Name the blood parasite species.
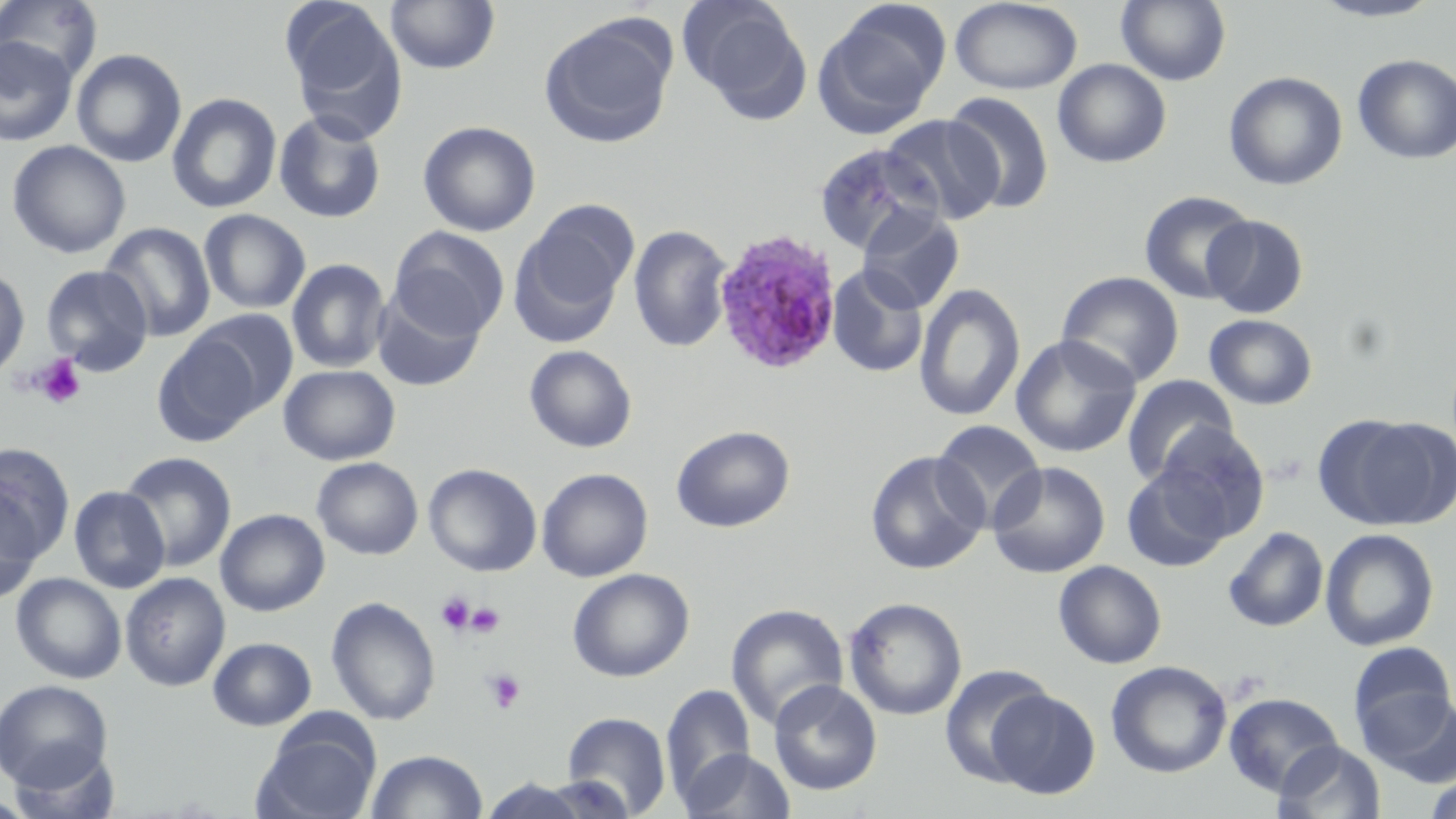
Plasmodium ovale.

Approximate bounding boxes as named x1/y1/x2/y2 corners in pixels. Uninfected red blood cell locations: (x1=0, y1=0, x2=103, y2=83), (x1=281, y1=0, x2=409, y2=142), (x1=385, y1=0, x2=500, y2=75), (x1=1116, y1=0, x2=1231, y2=85), (x1=1308, y1=0, x2=1446, y2=23), (x1=678, y1=1, x2=812, y2=118), (x1=813, y1=1, x2=950, y2=136), (x1=950, y1=1, x2=1083, y2=95), (x1=539, y1=15, x2=677, y2=149), (x1=0, y1=36, x2=78, y2=146), (x1=71, y1=48, x2=187, y2=168), (x1=1353, y1=53, x2=1456, y2=164), (x1=1052, y1=58, x2=1172, y2=168), (x1=1223, y1=71, x2=1348, y2=190), (x1=167, y1=92, x2=282, y2=214), (x1=944, y1=92, x2=1055, y2=215), (x1=273, y1=110, x2=387, y2=224), (x1=881, y1=114, x2=1005, y2=225), (x1=417, y1=120, x2=541, y2=237), (x1=6, y1=140, x2=131, y2=259), (x1=813, y1=143, x2=941, y2=256), (x1=1138, y1=190, x2=1257, y2=304), (x1=857, y1=205, x2=965, y2=313), (x1=511, y1=206, x2=637, y2=343), (x1=199, y1=209, x2=311, y2=314), (x1=1202, y1=214, x2=1309, y2=319), (x1=100, y1=222, x2=216, y2=342), (x1=628, y1=224, x2=734, y2=353), (x1=389, y1=226, x2=509, y2=340), (x1=286, y1=258, x2=391, y2=373), (x1=41, y1=264, x2=153, y2=375), (x1=826, y1=264, x2=928, y2=378), (x1=0, y1=265, x2=30, y2=379), (x1=1056, y1=271, x2=1185, y2=388), (x1=914, y1=283, x2=1026, y2=422), (x1=371, y1=291, x2=485, y2=392), (x1=187, y1=309, x2=299, y2=417), (x1=1204, y1=314, x2=1317, y2=410), (x1=152, y1=334, x2=263, y2=446), (x1=1010, y1=334, x2=1142, y2=458), (x1=524, y1=344, x2=637, y2=453), (x1=279, y1=364, x2=400, y2=465), (x1=1121, y1=374, x2=1238, y2=485), (x1=1319, y1=414, x2=1454, y2=530), (x1=931, y1=420, x2=1046, y2=529), (x1=1153, y1=423, x2=1270, y2=541), (x1=671, y1=425, x2=795, y2=532), (x1=0, y1=444, x2=75, y2=560), (x1=119, y1=451, x2=236, y2=572), (x1=865, y1=451, x2=989, y2=574), (x1=312, y1=456, x2=423, y2=560), (x1=987, y1=460, x2=1111, y2=579), (x1=423, y1=463, x2=542, y2=576), (x1=1121, y1=465, x2=1232, y2=572), (x1=537, y1=468, x2=653, y2=582), (x1=68, y1=485, x2=169, y2=593), (x1=0, y1=489, x2=42, y2=604), (x1=215, y1=509, x2=329, y2=616), (x1=1223, y1=526, x2=1329, y2=632), (x1=1320, y1=528, x2=1439, y2=651), (x1=1053, y1=560, x2=1166, y2=669), (x1=567, y1=568, x2=694, y2=682), (x1=120, y1=572, x2=230, y2=691), (x1=11, y1=573, x2=127, y2=684), (x1=326, y1=596, x2=440, y2=725), (x1=844, y1=597, x2=967, y2=720), (x1=726, y1=603, x2=849, y2=730), (x1=207, y1=637, x2=317, y2=730), (x1=1348, y1=641, x2=1456, y2=743), (x1=1106, y1=660, x2=1232, y2=778), (x1=939, y1=665, x2=1054, y2=785), (x1=0, y1=679, x2=113, y2=791), (x1=768, y1=679, x2=882, y2=795), (x1=660, y1=684, x2=757, y2=806), (x1=984, y1=688, x2=1101, y2=799), (x1=1362, y1=689, x2=1456, y2=788), (x1=1224, y1=692, x2=1343, y2=796), (x1=561, y1=712, x2=672, y2=817), (x1=253, y1=721, x2=380, y2=819), (x1=1273, y1=740, x2=1386, y2=819), (x1=6, y1=744, x2=121, y2=819), (x1=366, y1=749, x2=488, y2=819), (x1=678, y1=749, x2=796, y2=819), (x1=1424, y1=773, x2=1456, y2=819), (x1=470, y1=777, x2=616, y2=818). Plasmodium ovale-infected red blood cell locations: (x1=711, y1=227, x2=843, y2=376). Platelet locations: (x1=32, y1=355, x2=87, y2=409), (x1=436, y1=591, x2=475, y2=634), (x1=466, y1=602, x2=505, y2=637), (x1=484, y1=669, x2=526, y2=714). One field of a larger specimen. Thin blood film. 1000x magnification. May-Grünwald-Giemsa-stained preparation. Light microscopy. Image is 1456×819 pixels.